Identify the blood parasite species.
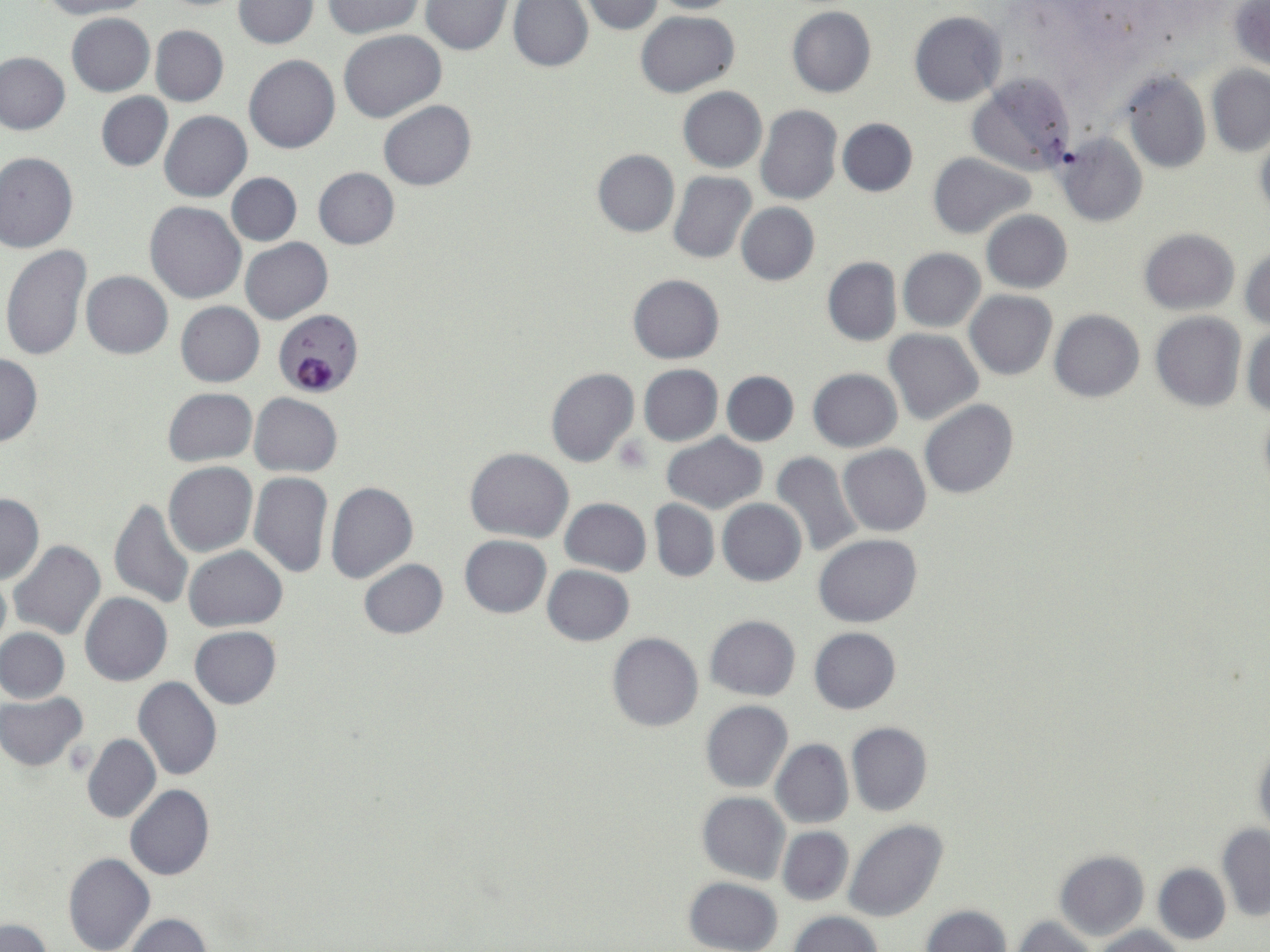

Plasmodium falciparum.

Approximate bounding boxes as [x1, y1, x2, y2] in pixels. Platelet locations: [613, 436, 651, 474]. Uninfected red blood cell locations: [38, 0, 149, 20], [232, 0, 319, 49], [645, 0, 745, 13], [323, 1, 426, 41], [508, 1, 592, 72], [577, 1, 666, 34], [420, 2, 512, 55], [1229, 3, 1270, 72], [786, 7, 876, 98], [635, 10, 740, 99], [909, 11, 1006, 107], [65, 13, 155, 97], [150, 25, 227, 107], [338, 30, 446, 122], [0, 52, 71, 134], [244, 55, 340, 154], [1207, 65, 1270, 156], [966, 72, 1077, 176], [1119, 72, 1211, 174], [678, 87, 767, 172], [96, 92, 172, 171], [378, 101, 476, 190], [756, 105, 842, 205], [160, 110, 252, 201], [837, 118, 918, 196], [1055, 134, 1148, 226], [1253, 134, 1270, 223], [592, 150, 679, 237], [0, 152, 78, 253], [927, 152, 1036, 239], [591, 163, 754, 253], [313, 167, 399, 248], [667, 171, 757, 265], [227, 172, 303, 246], [146, 202, 246, 303], [735, 203, 819, 285], [982, 210, 1072, 293], [1140, 228, 1239, 314], [241, 238, 333, 325], [1, 244, 92, 362], [1241, 247, 1270, 329], [898, 248, 985, 332], [822, 257, 901, 346], [82, 271, 173, 358], [628, 274, 725, 363], [965, 291, 1058, 380], [175, 302, 265, 387], [1049, 309, 1145, 402], [1150, 312, 1247, 412], [1243, 326, 1270, 418], [883, 329, 982, 424], [0, 356, 43, 446], [637, 365, 723, 446], [545, 368, 639, 468], [808, 368, 902, 452], [721, 371, 799, 446], [162, 387, 257, 467], [250, 394, 342, 476], [919, 400, 1020, 499], [662, 433, 767, 514], [838, 445, 932, 536], [465, 448, 574, 543], [768, 451, 864, 557], [164, 462, 257, 558], [249, 473, 333, 578], [325, 481, 418, 584], [0, 492, 44, 583], [110, 496, 193, 613], [561, 498, 651, 576], [718, 499, 806, 586], [649, 500, 719, 580], [813, 534, 921, 628], [459, 535, 551, 618], [9, 541, 106, 641], [185, 546, 287, 631], [357, 559, 449, 639], [542, 565, 635, 645], [0, 571, 10, 660], [80, 592, 172, 685], [704, 615, 801, 701], [189, 626, 282, 708], [808, 627, 901, 714], [0, 628, 70, 704], [607, 632, 703, 733], [134, 677, 222, 780], [1, 692, 88, 771], [700, 700, 793, 793], [847, 722, 933, 817], [82, 734, 161, 824], [1251, 737, 1270, 840], [771, 739, 854, 828], [126, 784, 215, 880], [697, 792, 790, 884], [843, 818, 950, 921], [1216, 824, 1269, 922], [777, 827, 853, 906], [1054, 850, 1149, 942], [63, 852, 156, 952], [1153, 862, 1231, 947], [683, 876, 783, 952], [918, 904, 1013, 952], [788, 911, 882, 952], [120, 913, 212, 952], [1011, 914, 1100, 952], [2, 919, 53, 952], [1090, 926, 1188, 951]. Plasmodium falciparum-infected red blood cell locations: [273, 311, 362, 398]. Thin blood film. Captured at 1000x magnification. May-Grünwald-Giemsa stain. Image is 1270×952 pixels. One field of a larger specimen. Light microscopy.